Name the parasite shown.
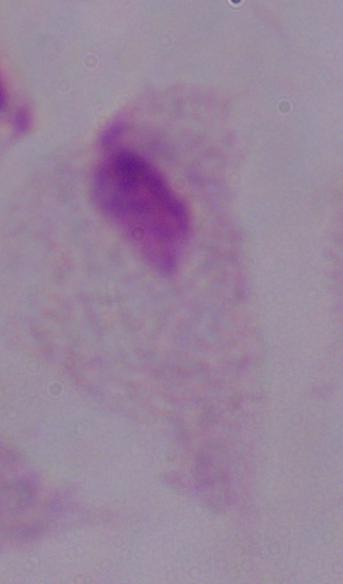

A trichomonad.

1000x magnification. Micrograph.